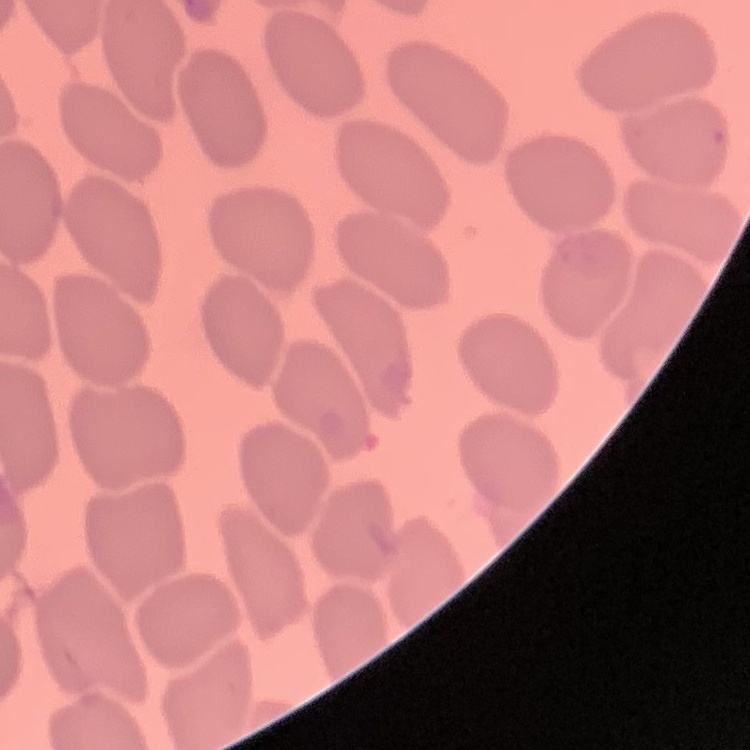
The red blood cells exhibit no rouleaux formation. Thin blood smear. One tile cut from a larger photomicrograph. Stained with either Field's or Giemsa.